Name the blood parasite species.
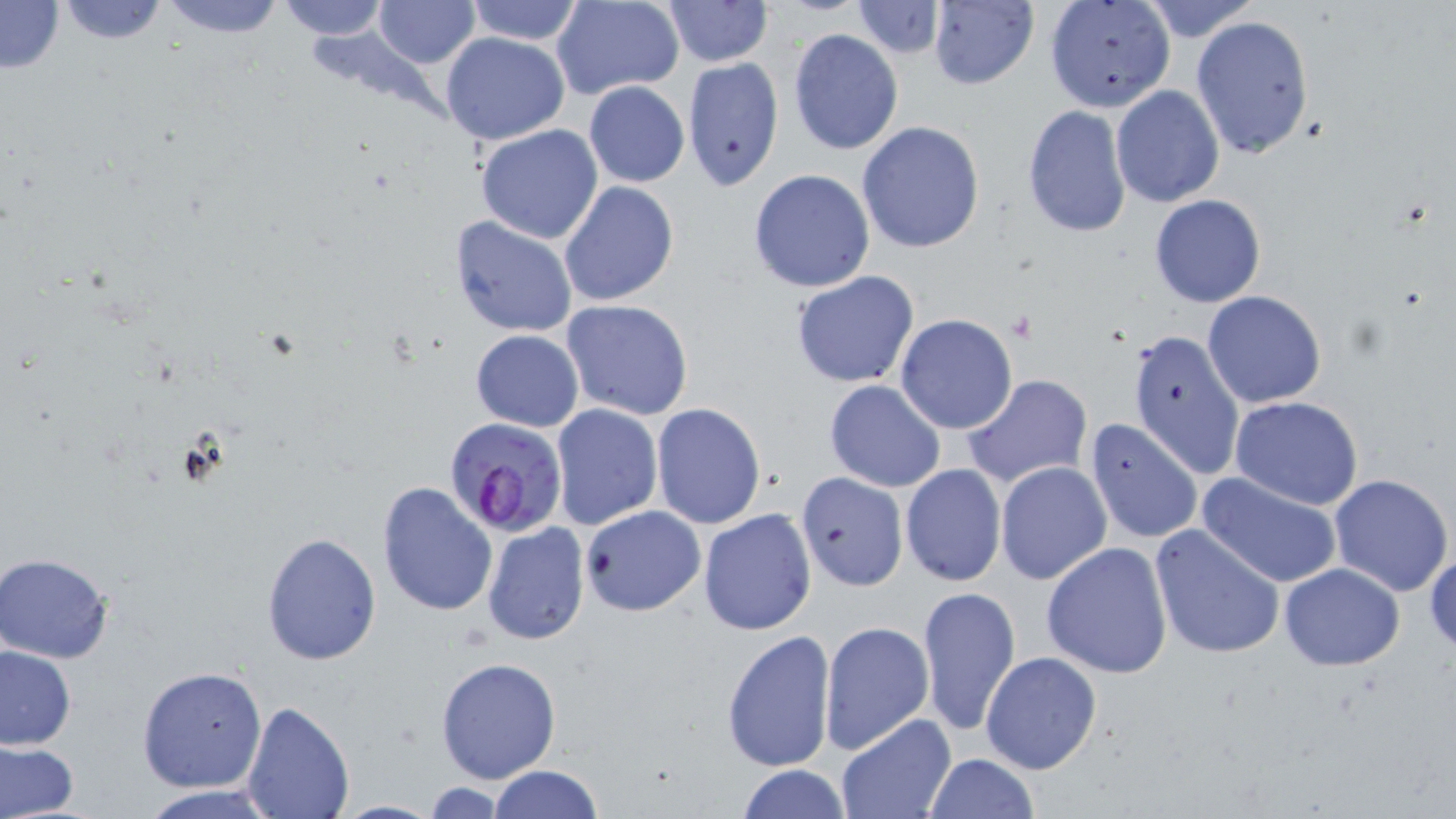
Plasmodium falciparum.

image size = 1456×819 pixels
modality = light microscopy
field of view = one of a larger specimen
uninfected red blood cell locations = approximate bounding boxes as (x1,y1)-(x2,y2) corner pairs in pixels: (56,0)-(171,47), (151,0)-(291,39), (273,0)-(392,41), (464,0)-(585,45), (551,0)-(685,101), (928,0)-(1038,91), (1135,0)-(1262,43), (0,1)-(65,75), (371,1)-(481,69), (850,1)-(945,58), (1043,1)-(1176,112), (657,2)-(774,69), (1191,14)-(1315,158), (788,28)-(902,154), (440,31)-(571,145), (682,58)-(785,189), (583,80)-(690,188), (1111,84)-(1225,208), (1021,105)-(1132,239), (856,122)-(986,252), (475,125)-(604,245), (748,168)-(876,294), (558,181)-(679,307), (1149,194)-(1265,307), (449,215)-(579,338), (791,271)-(921,388), (1202,290)-(1327,408), (560,299)-(695,422), (895,313)-(1018,435), (1127,328)-(1246,482), (470,330)-(583,431), (963,374)-(1093,491), (824,379)-(945,492), (1230,395)-(1365,509), (651,403)-(766,530), (550,404)-(664,531), (1082,417)-(1204,543), (995,461)-(1113,586), (900,464)-(1006,586), (796,471)-(908,591), (1196,472)-(1345,588), (1329,473)-(1453,595), (376,480)-(499,618), (579,505)-(705,616), (699,508)-(817,633), (481,522)-(591,646), (1150,523)-(1285,659), (260,533)-(382,665), (1042,542)-(1173,678), (1425,547)-(1456,658), (1,554)-(115,664), (1279,563)-(1404,670), (917,585)-(1019,736), (819,619)-(934,756), (721,629)-(835,772), (0,645)-(76,750), (980,651)-(1103,776), (435,657)-(562,784), (138,666)-(268,794), (242,700)-(354,818), (835,714)-(955,819), (0,740)-(80,817), (923,753)-(1039,818), (736,765)-(852,819), (489,766)-(602,819), (417,781)-(514,816), (136,786)-(281,819)
Plasmodium falciparum-infected red blood cell locations = approximate bounding boxes as (x1,y1)-(x2,y2) corner pairs in pixels: (442,416)-(569,540)
magnification = 1000x
stain = May-Grünwald-Giemsa
preparation = thin blood film